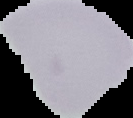 Segmented cell region on a black background. Result: negative for Plasmodium parasites. Image is 133×118 pixels. From a thin blood film.